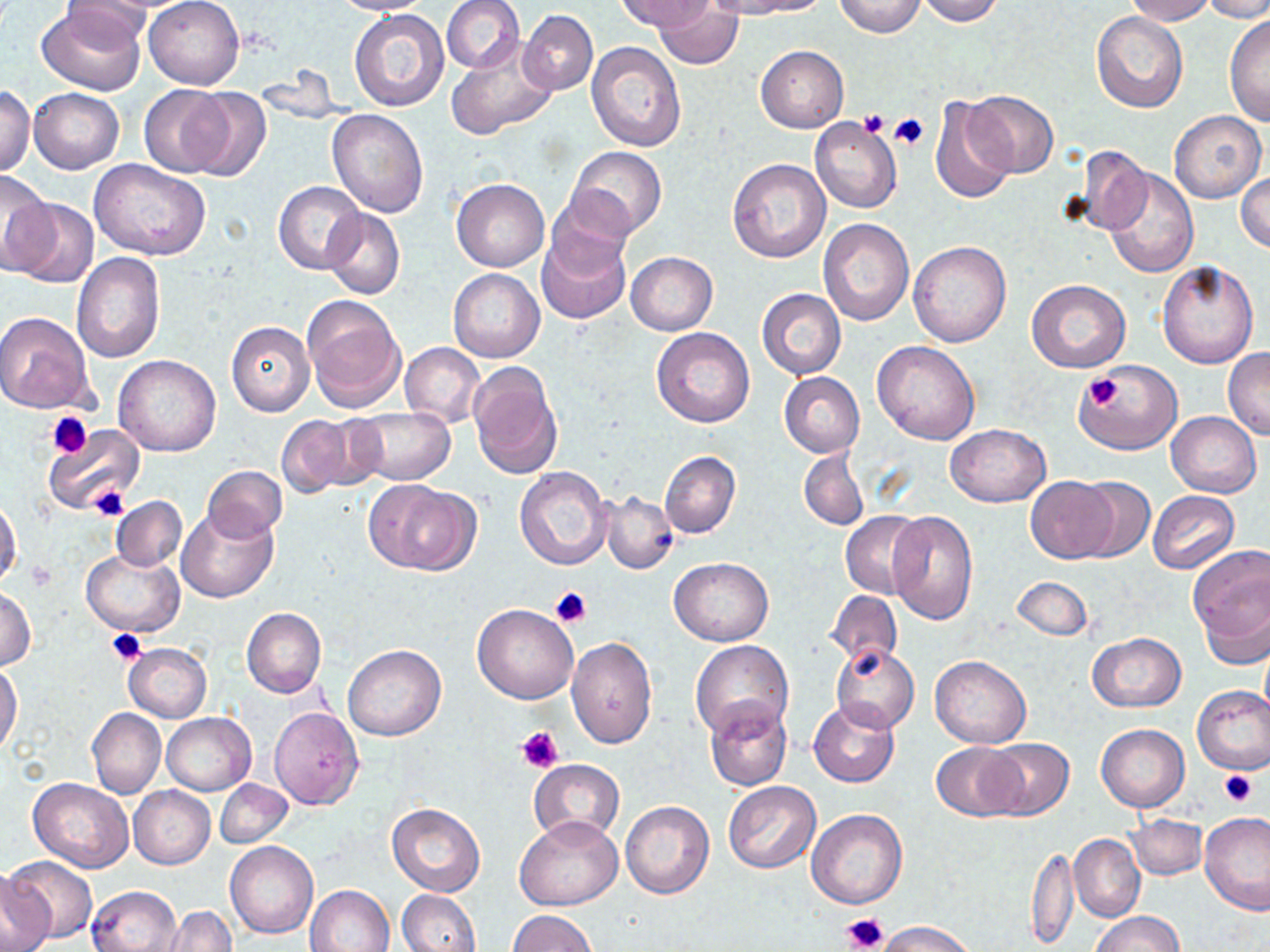 Approximate bounding boxes as named x1/y1/x2/y2 corners in pixels. Platelet locations: (x1=857, y1=111, x2=890, y2=136), (x1=889, y1=111, x2=929, y2=152), (x1=1083, y1=374, x2=1124, y2=411), (x1=47, y1=412, x2=92, y2=458), (x1=86, y1=485, x2=129, y2=520), (x1=27, y1=561, x2=58, y2=590), (x1=550, y1=586, x2=591, y2=628), (x1=106, y1=630, x2=149, y2=664), (x1=515, y1=726, x2=563, y2=775), (x1=1218, y1=770, x2=1257, y2=806), (x1=842, y1=912, x2=890, y2=951). Uninfected red blood cell locations: (x1=145, y1=0, x2=243, y2=88), (x1=329, y1=0, x2=432, y2=15), (x1=441, y1=0, x2=524, y2=73), (x1=616, y1=0, x2=711, y2=33), (x1=734, y1=0, x2=830, y2=17), (x1=835, y1=0, x2=927, y2=38), (x1=914, y1=0, x2=1005, y2=25), (x1=1124, y1=0, x2=1216, y2=24), (x1=1203, y1=0, x2=1270, y2=23), (x1=64, y1=1, x2=153, y2=49), (x1=653, y1=2, x2=743, y2=70), (x1=36, y1=5, x2=145, y2=95), (x1=349, y1=8, x2=450, y2=112), (x1=519, y1=10, x2=598, y2=95), (x1=1091, y1=12, x2=1188, y2=114), (x1=1225, y1=15, x2=1269, y2=129), (x1=446, y1=35, x2=560, y2=141), (x1=586, y1=41, x2=686, y2=151), (x1=755, y1=45, x2=848, y2=132), (x1=138, y1=84, x2=231, y2=176), (x1=183, y1=86, x2=272, y2=182), (x1=1, y1=87, x2=36, y2=176), (x1=28, y1=88, x2=123, y2=174), (x1=966, y1=90, x2=1059, y2=176), (x1=930, y1=95, x2=1018, y2=203), (x1=326, y1=109, x2=428, y2=217), (x1=1168, y1=110, x2=1266, y2=202), (x1=809, y1=117, x2=902, y2=214), (x1=567, y1=146, x2=667, y2=237), (x1=1069, y1=147, x2=1152, y2=236), (x1=89, y1=159, x2=211, y2=262), (x1=727, y1=159, x2=831, y2=263), (x1=1103, y1=168, x2=1198, y2=279), (x1=0, y1=169, x2=55, y2=274), (x1=1236, y1=172, x2=1270, y2=253), (x1=452, y1=178, x2=549, y2=272), (x1=273, y1=180, x2=366, y2=274), (x1=548, y1=185, x2=638, y2=277), (x1=8, y1=200, x2=98, y2=287), (x1=322, y1=207, x2=404, y2=299), (x1=817, y1=219, x2=914, y2=326), (x1=538, y1=227, x2=631, y2=324), (x1=907, y1=241, x2=1011, y2=348), (x1=72, y1=251, x2=166, y2=363), (x1=625, y1=251, x2=718, y2=335), (x1=1157, y1=260, x2=1259, y2=368), (x1=448, y1=269, x2=545, y2=362), (x1=1026, y1=280, x2=1130, y2=373), (x1=756, y1=289, x2=845, y2=379), (x1=302, y1=295, x2=406, y2=413), (x1=0, y1=311, x2=95, y2=413), (x1=226, y1=321, x2=315, y2=416), (x1=652, y1=328, x2=755, y2=427), (x1=872, y1=341, x2=979, y2=445), (x1=400, y1=342, x2=485, y2=429), (x1=1223, y1=349, x2=1270, y2=438), (x1=113, y1=356, x2=221, y2=457), (x1=467, y1=361, x2=562, y2=479), (x1=1079, y1=362, x2=1181, y2=454), (x1=779, y1=372, x2=864, y2=458), (x1=349, y1=407, x2=455, y2=484), (x1=1166, y1=411, x2=1261, y2=498), (x1=276, y1=414, x2=368, y2=497), (x1=946, y1=423, x2=1050, y2=507), (x1=42, y1=424, x2=145, y2=517), (x1=798, y1=448, x2=869, y2=531), (x1=660, y1=451, x2=739, y2=538), (x1=200, y1=465, x2=288, y2=541), (x1=515, y1=466, x2=612, y2=569), (x1=1026, y1=476, x2=1117, y2=563), (x1=1071, y1=476, x2=1155, y2=564), (x1=366, y1=480, x2=476, y2=576), (x1=1148, y1=490, x2=1240, y2=575), (x1=601, y1=492, x2=677, y2=574), (x1=109, y1=496, x2=187, y2=571), (x1=0, y1=497, x2=20, y2=589), (x1=176, y1=506, x2=279, y2=603), (x1=840, y1=511, x2=926, y2=599), (x1=887, y1=511, x2=978, y2=625), (x1=1185, y1=544, x2=1270, y2=661), (x1=81, y1=549, x2=185, y2=637), (x1=668, y1=557, x2=772, y2=645), (x1=1012, y1=576, x2=1093, y2=640), (x1=1, y1=585, x2=36, y2=670), (x1=826, y1=590, x2=901, y2=669), (x1=472, y1=603, x2=578, y2=704), (x1=241, y1=607, x2=326, y2=697), (x1=1087, y1=633, x2=1186, y2=712), (x1=567, y1=637, x2=657, y2=748), (x1=689, y1=640, x2=793, y2=741), (x1=123, y1=643, x2=211, y2=722), (x1=344, y1=644, x2=445, y2=741), (x1=831, y1=645, x2=920, y2=732), (x1=929, y1=654, x2=1031, y2=748), (x1=1, y1=663, x2=22, y2=757), (x1=1192, y1=684, x2=1270, y2=775), (x1=705, y1=698, x2=793, y2=791), (x1=810, y1=699, x2=899, y2=787), (x1=269, y1=706, x2=363, y2=809), (x1=87, y1=708, x2=166, y2=799), (x1=162, y1=713, x2=256, y2=796), (x1=1096, y1=723, x2=1190, y2=812), (x1=984, y1=737, x2=1075, y2=820), (x1=931, y1=742, x2=1024, y2=822), (x1=529, y1=758, x2=625, y2=847), (x1=28, y1=777, x2=134, y2=872), (x1=215, y1=779, x2=293, y2=848), (x1=723, y1=782, x2=820, y2=874), (x1=128, y1=786, x2=215, y2=869), (x1=621, y1=801, x2=714, y2=899), (x1=387, y1=803, x2=485, y2=896), (x1=806, y1=808, x2=907, y2=910), (x1=1199, y1=812, x2=1270, y2=916), (x1=1125, y1=813, x2=1206, y2=880), (x1=514, y1=814, x2=623, y2=910), (x1=1070, y1=834, x2=1145, y2=922), (x1=225, y1=841, x2=318, y2=939), (x1=1025, y1=842, x2=1078, y2=949), (x1=6, y1=855, x2=97, y2=943), (x1=0, y1=867, x2=55, y2=952), (x1=307, y1=884, x2=395, y2=951), (x1=87, y1=885, x2=182, y2=952), (x1=396, y1=889, x2=481, y2=952), (x1=160, y1=906, x2=236, y2=952), (x1=508, y1=910, x2=596, y2=952), (x1=1091, y1=911, x2=1186, y2=952), (x1=877, y1=920, x2=975, y2=952). Slide-level diagnosis: no evidence of blood parasites. One field of a larger specimen. Thin blood smear. Image is 1270×952 pixels. May-Grünwald-Giemsa-stained preparation. Captured at 1000x magnification. Light microscopy.